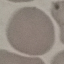 Result: no malaria parasites detected. Cell patch, automatically extracted from a larger field of view and resized to 64 × 64 pixels. Acquired by smartphone through the microscope eyepiece. Thin smear of blood. Giemsa-stained preparation.